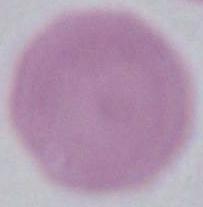

Summary:
  - Modality: micrograph
  - Magnification: 1000x
  - Identification: erythrocyte